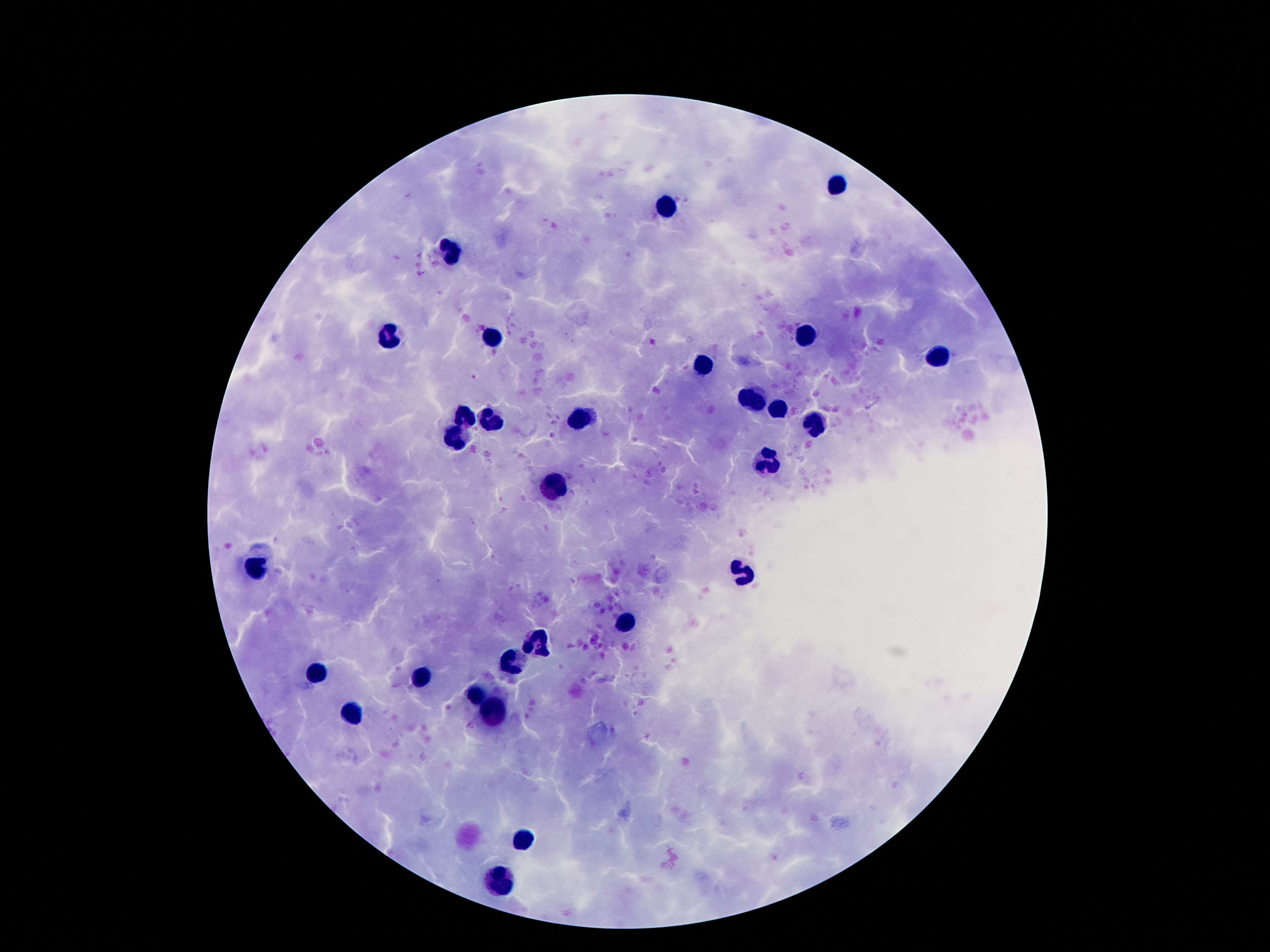
Approximate object centers, in pixels from the top-left corner. Leukocyte locations: (x=839, y=182), (x=666, y=206), (x=451, y=251), (x=390, y=334), (x=804, y=335), (x=491, y=339), (x=938, y=359), (x=704, y=367), (x=753, y=404), (x=778, y=411), (x=580, y=417), (x=463, y=419), (x=491, y=422), (x=815, y=424), (x=456, y=436), (x=768, y=461), (x=558, y=490), (x=256, y=566), (x=745, y=577), (x=622, y=624), (x=538, y=644), (x=510, y=664), (x=316, y=673), (x=417, y=679), (x=476, y=700), (x=498, y=713), (x=352, y=715), (x=523, y=839), (x=501, y=885). 100x magnification. Smartphone photograph taken through the microscope eyepiece. Giemsa-stained preparation. Image is 1270×952 pixels. Patient malaria status: negative. Single field of view. Thick blood film.